State the blood parasite species.
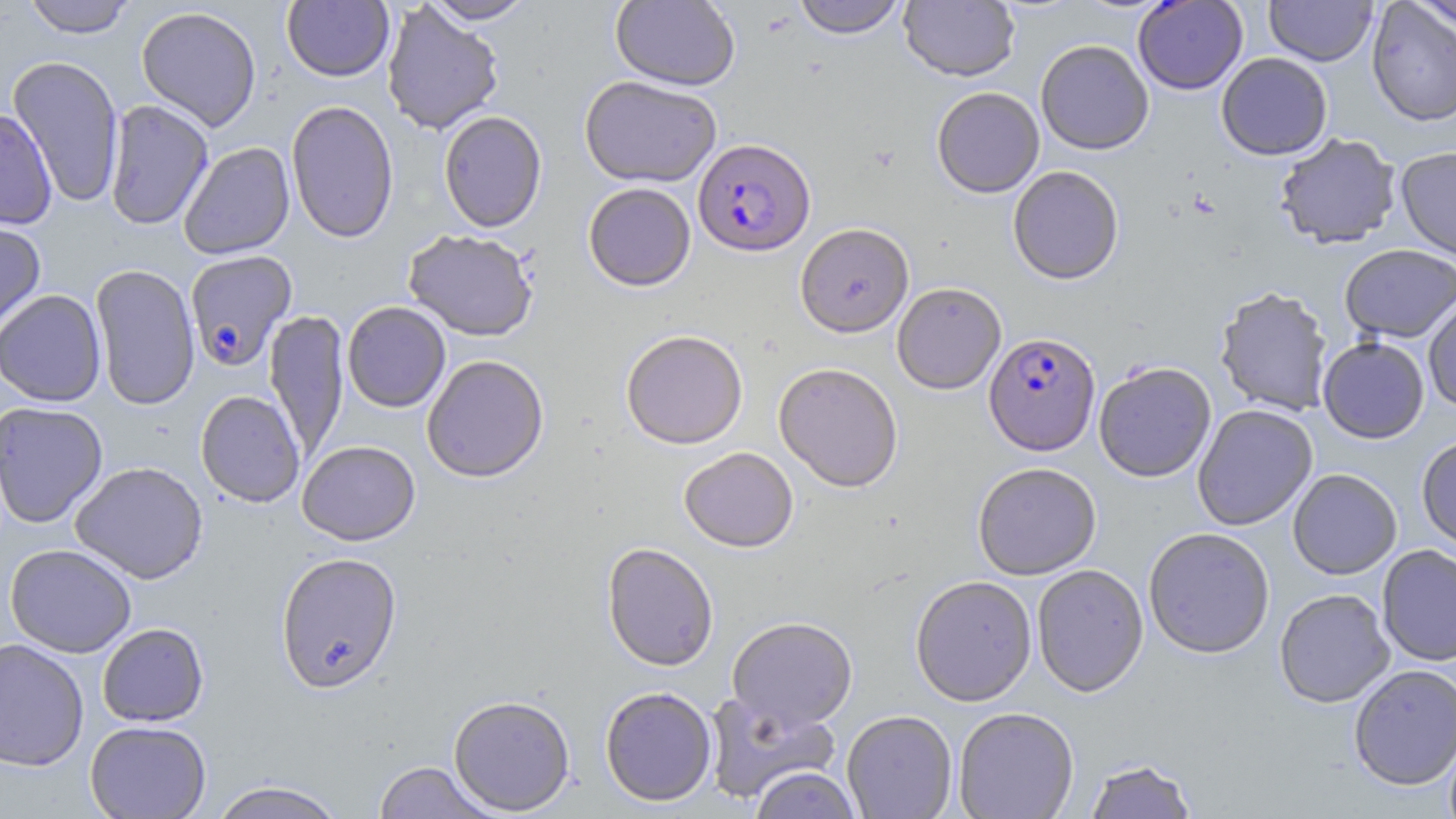

Plasmodium falciparum.

Approximate bounding boxes as (x1,y1)-(x2,y2) corner pairs in pixels. Uninfected red blood cell locations: (23,0)-(136,38), (421,0)-(535,24), (610,0)-(740,90), (792,0)-(907,39), (1264,0)-(1377,66), (1411,0)-(1455,36), (282,1)-(394,82), (900,1)-(1019,82), (1132,1)-(1248,94), (1366,1)-(1456,127), (381,3)-(504,135), (136,6)-(262,132), (1035,39)-(1154,155), (1216,52)-(1332,160), (7,56)-(125,207), (579,75)-(722,188), (931,86)-(1044,198), (104,99)-(213,230), (285,100)-(399,244), (0,108)-(57,229), (438,111)-(547,232), (1273,133)-(1401,249), (178,142)-(295,259), (1395,145)-(1456,262), (1007,165)-(1124,285), (583,183)-(696,291), (0,217)-(46,334), (795,223)-(914,338), (403,229)-(539,341), (1339,243)-(1456,343), (90,264)-(200,410), (892,282)-(1007,394), (1214,286)-(1334,417), (0,289)-(106,406), (1422,293)-(1456,414), (342,302)-(451,413), (264,309)-(349,463), (621,329)-(748,450), (1318,337)-(1430,443), (421,354)-(549,483), (1093,361)-(1216,482), (773,362)-(903,492), (195,390)-(305,508), (0,401)-(109,528), (1192,404)-(1318,531), (1416,435)-(1456,554), (297,440)-(420,545), (679,447)-(798,552), (70,461)-(209,584), (972,461)-(1102,579), (1288,468)-(1402,579), (1143,527)-(1275,659), (5,543)-(137,658), (601,543)-(719,672), (1376,544)-(1456,667), (275,552)-(403,694), (1031,564)-(1148,697), (910,575)-(1037,706), (1274,589)-(1395,708), (727,616)-(858,731), (97,622)-(209,727), (0,638)-(89,771), (1348,664)-(1456,791), (599,686)-(717,807), (702,691)-(841,804), (448,695)-(576,815), (953,707)-(1079,819), (842,710)-(957,819), (85,720)-(211,819), (1083,759)-(1199,819), (373,761)-(498,819), (748,767)-(862,819), (208,781)-(347,819). Plasmodium falciparum-infected red blood cell locations: (693,138)-(816,256), (184,250)-(298,371), (984,331)-(1100,455). May-Grünwald-Giemsa stain. One field of a larger specimen. Light microscopy. Image is 1456×819 pixels. Thin blood film. Captured at 1000x magnification.